Give the position of every malaria parasite and every leukocyte.
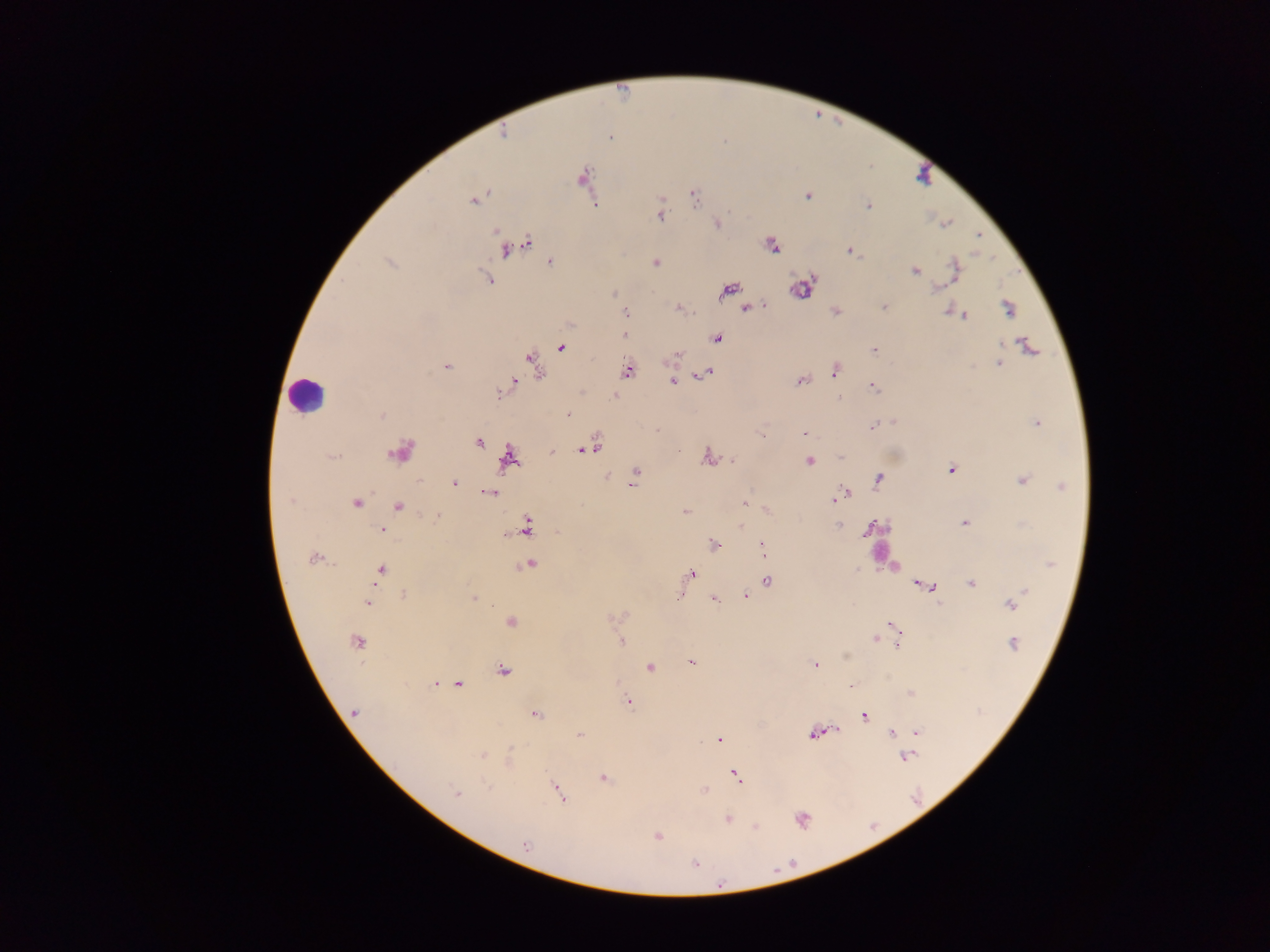
Approximate centers as [x, y] in pixels.
Malaria parasites: [503, 134], [610, 137], [583, 177], [807, 195], [694, 196], [474, 201], [868, 206], [660, 216], [947, 223], [718, 224], [978, 236], [527, 244], [771, 245], [506, 249], [851, 251], [550, 262], [655, 262], [390, 263], [955, 270], [915, 271], [487, 279], [803, 287], [938, 288], [729, 290], [614, 293], [764, 306], [884, 307], [746, 308], [678, 309], [1008, 309], [835, 311], [948, 312], [626, 313], [964, 315], [625, 334], [716, 338], [1027, 345], [561, 347], [874, 350], [677, 355], [532, 361], [998, 364], [446, 366], [835, 370], [628, 371], [707, 373], [800, 380], [672, 381], [512, 382], [873, 388], [614, 396], [839, 397], [382, 415], [568, 415], [893, 421], [1036, 423], [872, 427], [805, 434], [762, 436], [479, 443], [587, 450], [401, 452], [552, 452], [333, 456], [708, 457], [509, 458], [841, 459], [732, 460], [810, 461], [951, 469], [637, 471], [607, 476], [879, 478], [1022, 480], [453, 483], [633, 483], [1062, 487], [490, 492], [845, 493], [839, 497], [290, 501], [356, 503], [745, 503], [398, 507], [685, 512], [437, 516], [964, 523], [838, 524], [526, 526], [741, 526], [382, 530], [865, 532], [713, 545], [763, 550], [313, 559], [1050, 564], [529, 565], [381, 571], [691, 574], [767, 581], [918, 584], [972, 584], [932, 587], [1023, 591], [404, 595], [678, 595], [746, 596], [473, 598], [714, 599], [367, 603], [939, 604], [1012, 604], [511, 622], [892, 625], [875, 639], [621, 641], [357, 642], [1014, 644], [898, 645], [846, 657], [691, 661], [815, 665], [650, 667], [503, 671], [435, 684], [459, 684], [628, 701], [354, 712], [537, 714], [864, 715], [918, 732], [891, 733], [815, 734], [580, 735], [720, 739], [483, 755], [907, 757], [737, 776], [604, 779], [486, 785], [703, 791], [559, 792], [457, 793], [728, 819], [802, 820], [756, 826], [657, 836], [525, 845], [695, 864].
Leukocytes: [306, 394], [880, 551].

field of view = single
image size = 1270×952 pixels
preparation = thick blood film
capture = mobile-phone photograph through a microscope
country = Ghana